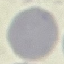

Summary:
  - Result: no malaria parasites seen
  - Stain: Giemsa
  - Image type: automatically extracted cell patch, resized to 64 × 64 pixels
  - Capture: smartphone camera at the microscope eyepiece
  - Preparation: thin smear